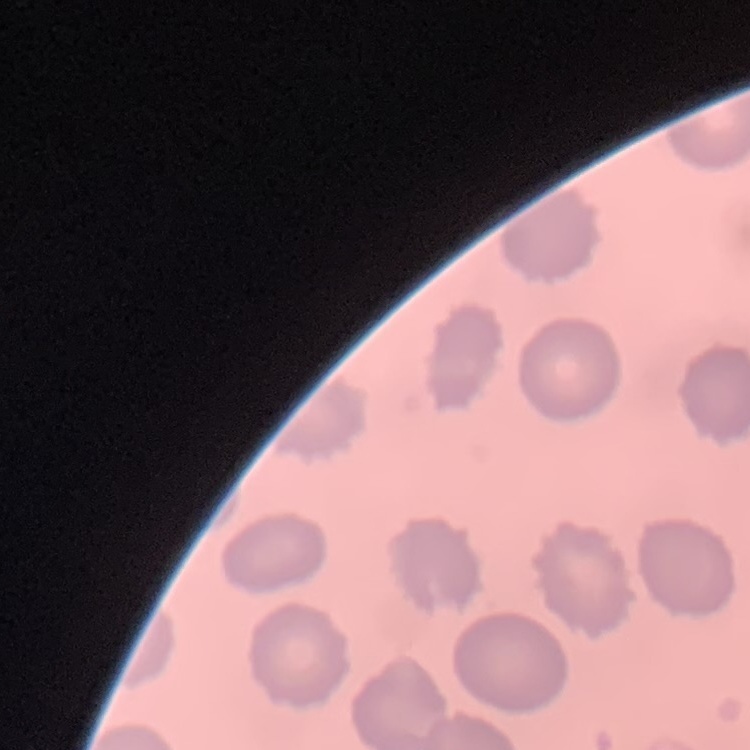
The erythrocytes exhibit no rouleaux formation. Thin blood film. Field's or Giemsa stain. One tile cut from a larger photomicrograph.